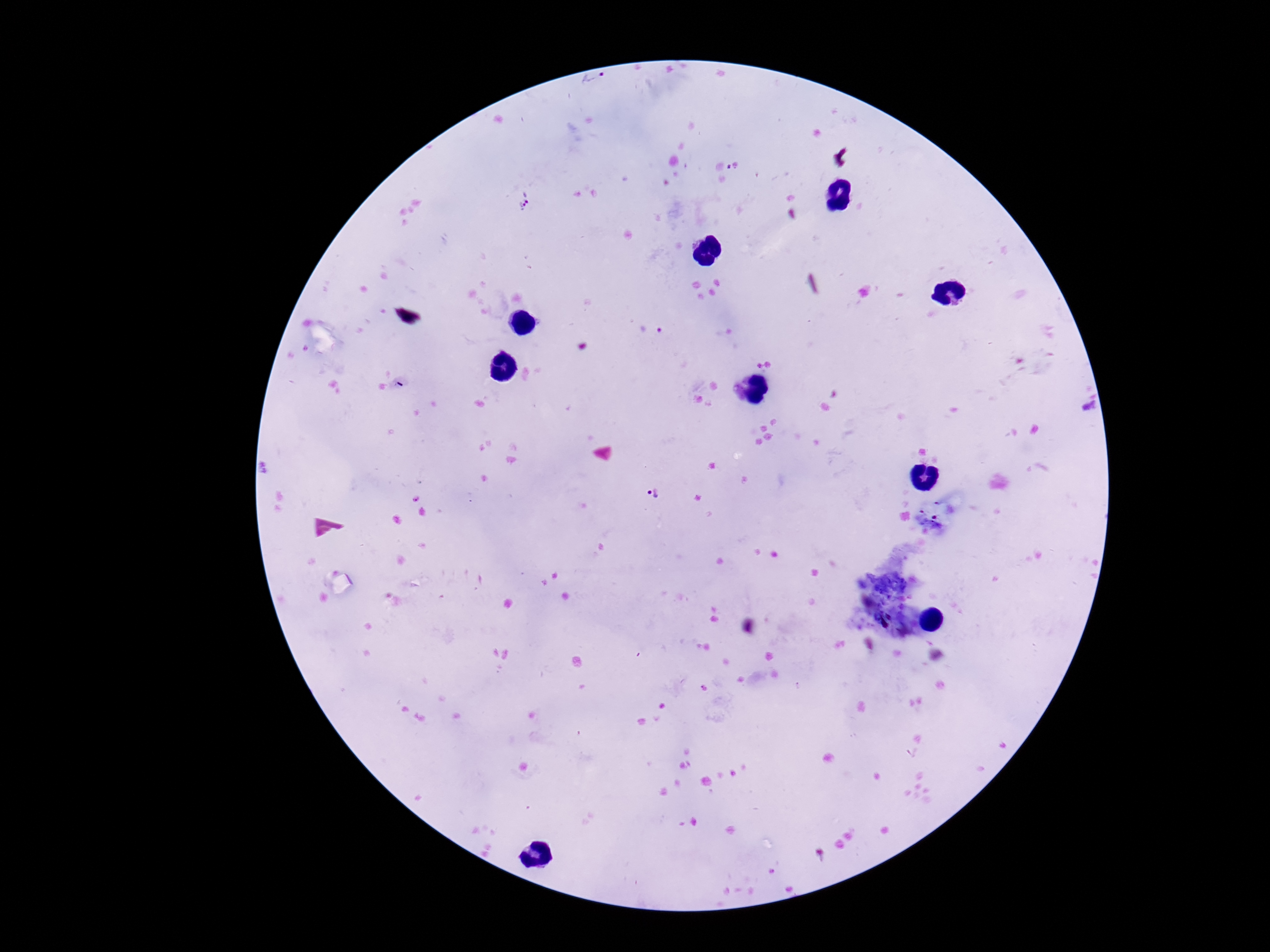 Approximate object centers, in pixels from the top-left corner. Plasmodium parasite locations: (x=595, y=81), (x=523, y=204), (x=651, y=328), (x=655, y=493). Photographed through the microscope eyepiece with a smartphone camera. Single field of view. Image is 1270×952 pixels. Giemsa stain. Thick blood smear. 100x magnification. Patient malaria status: positive.